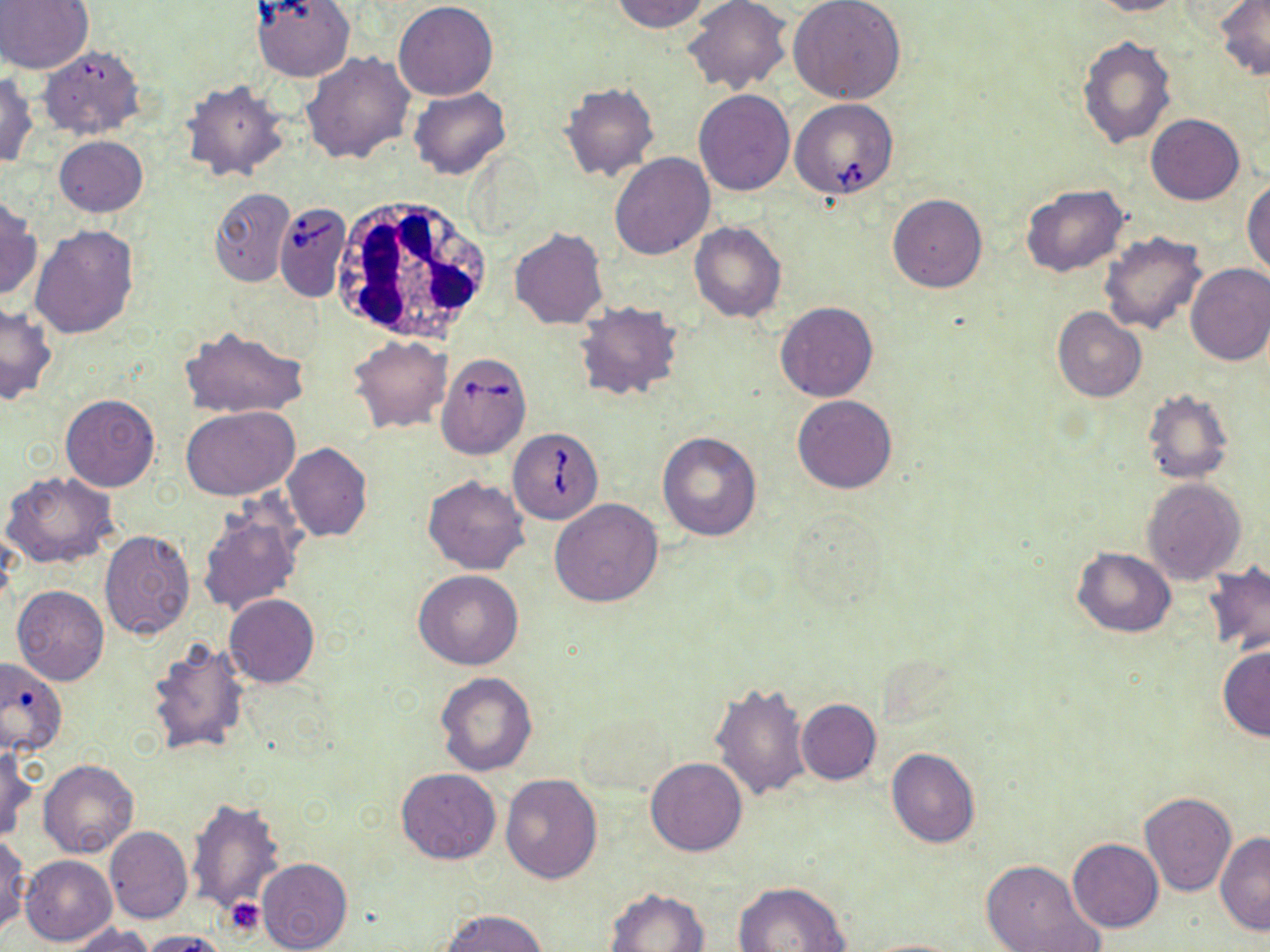
Summary:
  - Coordinate format: approximate bounding boxes as named x1/y1/x2/y2 corners in pixels
  - Uninfected red blood cell locations: (x1=0, y1=0, x2=92, y2=74), (x1=609, y1=0, x2=711, y2=33), (x1=683, y1=0, x2=792, y2=95), (x1=787, y1=0, x2=905, y2=105), (x1=1088, y1=0, x2=1187, y2=16), (x1=1215, y1=0, x2=1270, y2=80), (x1=251, y1=1, x2=356, y2=82), (x1=393, y1=1, x2=499, y2=100), (x1=1077, y1=37, x2=1176, y2=149), (x1=38, y1=46, x2=145, y2=140), (x1=302, y1=51, x2=414, y2=163), (x1=0, y1=73, x2=39, y2=168), (x1=180, y1=80, x2=291, y2=184), (x1=559, y1=81, x2=660, y2=182), (x1=409, y1=86, x2=511, y2=178), (x1=694, y1=89, x2=795, y2=196), (x1=571, y1=107, x2=686, y2=240), (x1=1145, y1=114, x2=1245, y2=205), (x1=53, y1=136, x2=147, y2=217), (x1=610, y1=152, x2=715, y2=258), (x1=1243, y1=178, x2=1270, y2=277), (x1=1020, y1=183, x2=1129, y2=277), (x1=209, y1=188, x2=293, y2=286), (x1=887, y1=193, x2=988, y2=292), (x1=0, y1=196, x2=41, y2=300), (x1=689, y1=221, x2=786, y2=324), (x1=31, y1=224, x2=140, y2=339), (x1=509, y1=228, x2=608, y2=329), (x1=1098, y1=231, x2=1208, y2=336), (x1=1184, y1=264, x2=1270, y2=366), (x1=775, y1=301, x2=878, y2=401), (x1=0, y1=303, x2=57, y2=405), (x1=574, y1=303, x2=684, y2=403), (x1=1051, y1=307, x2=1147, y2=402), (x1=180, y1=326, x2=308, y2=420), (x1=349, y1=336, x2=453, y2=433), (x1=1140, y1=388, x2=1235, y2=485), (x1=60, y1=394, x2=159, y2=492), (x1=792, y1=395, x2=898, y2=494), (x1=182, y1=405, x2=300, y2=499), (x1=657, y1=431, x2=762, y2=542), (x1=281, y1=443, x2=371, y2=542), (x1=1, y1=471, x2=118, y2=569), (x1=423, y1=475, x2=529, y2=574), (x1=1142, y1=477, x2=1248, y2=585), (x1=550, y1=497, x2=664, y2=607), (x1=197, y1=505, x2=305, y2=617), (x1=99, y1=530, x2=195, y2=639), (x1=1072, y1=547, x2=1175, y2=638), (x1=1200, y1=563, x2=1270, y2=655), (x1=414, y1=570, x2=524, y2=670), (x1=12, y1=586, x2=109, y2=686), (x1=224, y1=593, x2=320, y2=688), (x1=145, y1=635, x2=252, y2=756), (x1=1218, y1=646, x2=1270, y2=741), (x1=0, y1=657, x2=66, y2=757), (x1=436, y1=672, x2=537, y2=775), (x1=709, y1=681, x2=813, y2=801), (x1=795, y1=699, x2=881, y2=784), (x1=576, y1=709, x2=676, y2=795), (x1=885, y1=747, x2=980, y2=848), (x1=1, y1=748, x2=36, y2=841), (x1=645, y1=757, x2=747, y2=855), (x1=39, y1=759, x2=139, y2=858), (x1=397, y1=768, x2=500, y2=864), (x1=500, y1=774, x2=604, y2=883), (x1=1139, y1=792, x2=1237, y2=897), (x1=187, y1=797, x2=284, y2=914), (x1=104, y1=827, x2=192, y2=925), (x1=1215, y1=832, x2=1269, y2=935), (x1=0, y1=834, x2=29, y2=937), (x1=1067, y1=838, x2=1163, y2=932), (x1=20, y1=855, x2=116, y2=945), (x1=256, y1=857, x2=352, y2=952), (x1=979, y1=859, x2=1103, y2=952), (x1=732, y1=881, x2=850, y2=952), (x1=604, y1=887, x2=709, y2=951), (x1=440, y1=908, x2=549, y2=952), (x1=62, y1=924, x2=158, y2=952), (x1=137, y1=930, x2=231, y2=952), (x1=859, y1=937, x2=969, y2=951)
  - White blood cell locations: (x1=328, y1=197, x2=494, y2=346)
  - Platelet locations: (x1=224, y1=897, x2=264, y2=936)
  - Babesia divergens-infected red blood cell locations: (x1=791, y1=99, x2=899, y2=201), (x1=273, y1=202, x2=352, y2=301), (x1=435, y1=352, x2=532, y2=459), (x1=507, y1=428, x2=604, y2=523)
  - Slide-level diagnosis: Babesia divergens
  - Stain: May-Grünwald-Giemsa
  - Modality: optical microscopy
  - Preparation: thin blood smear
  - Field of view: single
  - Image size: 1270×952 pixels
  - Magnification: 1000x